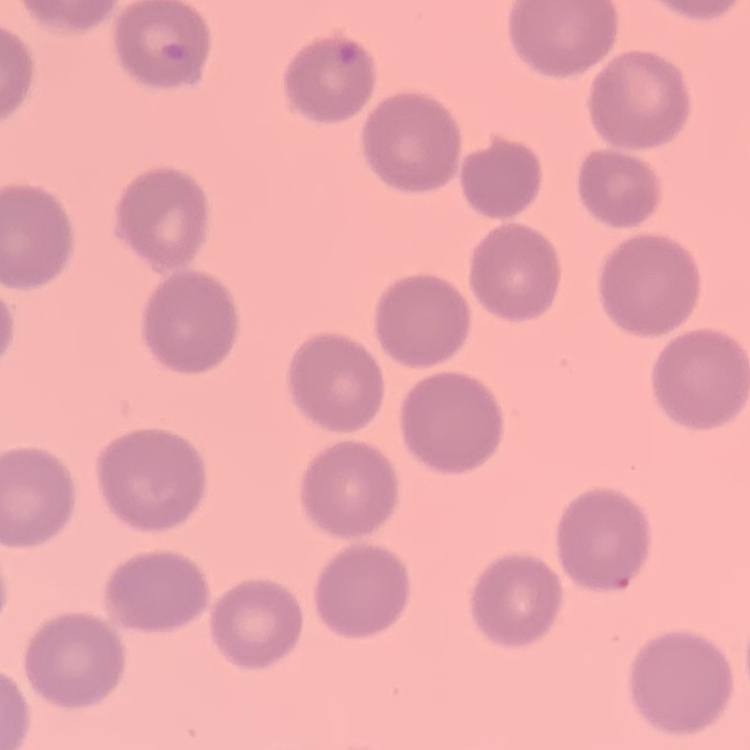

{
  "red_blood_cell_morphology": "no rouleaux formation",
  "stain": "Field's or Giemsa",
  "preparation": "thin blood film",
  "image_type": "square crop of a larger photomicrograph"
}